Assess this cell for malaria.
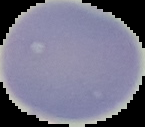

It is uninfected.

image type = cell region segmented out of the field of view; surrounding area masked to black
image size = 145×127 pixels
preparation = thin blood film